Report the malaria status of this cell.
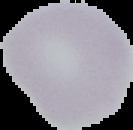
Uninfected.

{
  "image_size": "133×130 pixels",
  "image_type": "segmented cell region on a black background",
  "preparation": "thin blood smear"
}